Locate every blood parasite and identify its species.
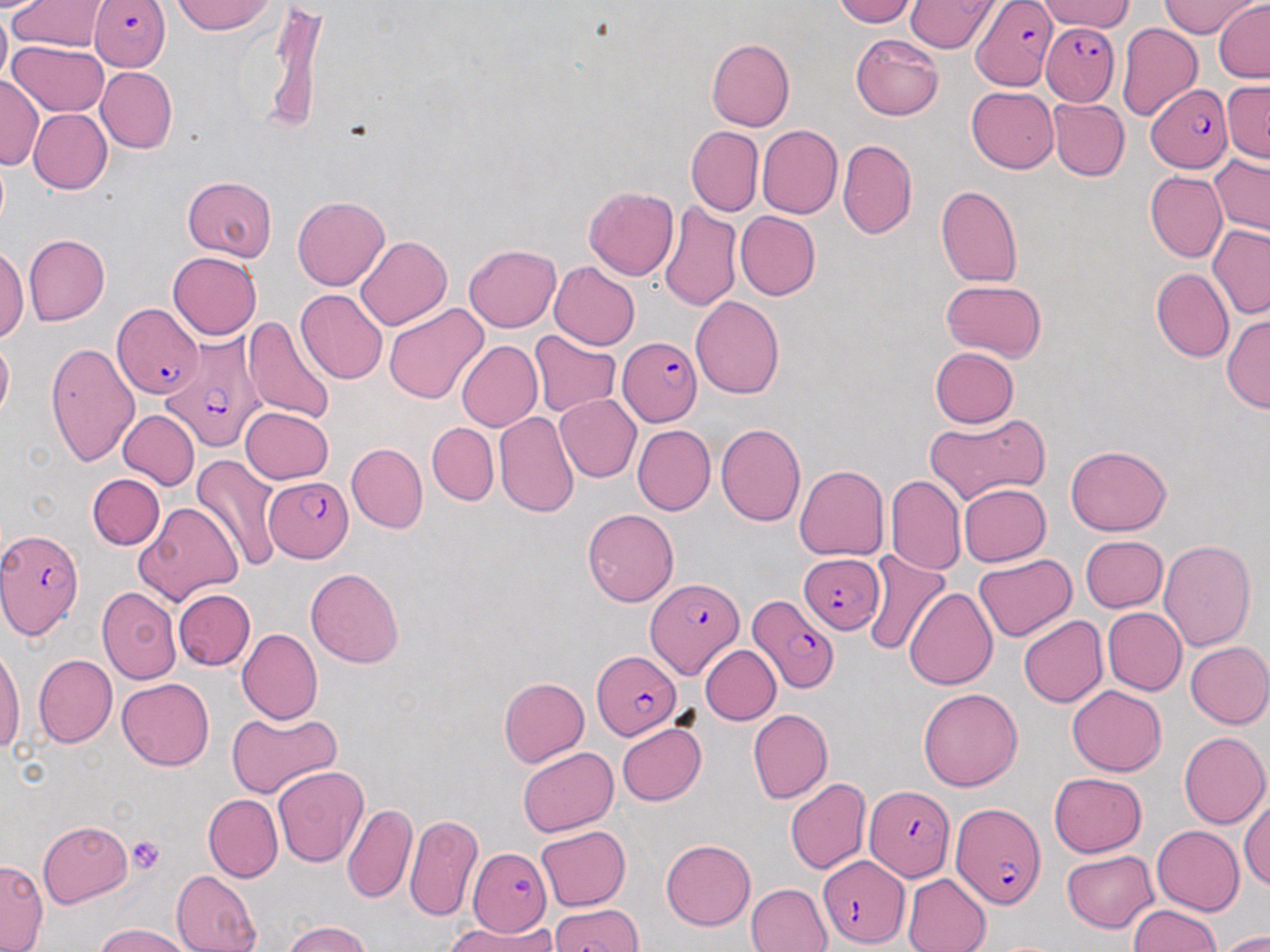

Approximate bounding boxes as (x1,y1)-(x2,y2) corner pairs in pixels.
Plasmodium falciparum-infected red blood cells: (970,0)-(1056,91), (91,1)-(171,72), (1040,20)-(1122,109), (1145,84)-(1234,173), (111,303)-(202,399), (160,336)-(264,453), (620,337)-(702,427), (267,478)-(353,559), (1,527)-(86,639), (798,553)-(884,633), (646,577)-(741,677), (748,592)-(839,693), (594,652)-(680,734), (865,786)-(952,882), (951,802)-(1046,907), (470,847)-(552,938), (820,855)-(909,948).
No Plasmodium ovale, Plasmodium malariae, Plasmodium vivax, Babesia divergens, or Trypanosoma brucei observed.

slide-level diagnosis = Plasmodium falciparum
image size = 1270×952 pixels
uninfected red blood cell locations = approximate bounding boxes as (x1,y1)-(x2,y2) corner pairs in pixels: (173,0)-(277,35), (833,0)-(918,26), (1161,0)-(1261,38), (1214,0)-(1270,82), (8,1)-(108,53), (905,1)-(998,52), (1035,2)-(1139,32), (0,4)-(11,91), (263,9)-(326,135), (1116,22)-(1203,121), (850,33)-(943,120), (706,38)-(794,131), (8,39)-(108,117), (96,66)-(177,154), (0,73)-(42,170), (1222,80)-(1270,163), (967,87)-(1058,173), (1048,97)-(1130,181), (28,109)-(112,194), (756,125)-(842,219), (685,126)-(764,216), (838,139)-(917,239), (1209,153)-(1270,236), (1145,171)-(1227,263), (183,177)-(277,260), (936,184)-(1022,287), (583,186)-(678,280), (293,196)-(389,290), (659,200)-(742,311), (735,211)-(821,300), (1207,225)-(1270,320), (23,235)-(109,326), (355,235)-(451,330), (464,243)-(561,332), (0,246)-(29,344), (167,251)-(262,340), (549,262)-(640,351), (1152,268)-(1234,362), (941,280)-(1047,360), (295,289)-(389,385), (689,295)-(785,398), (383,303)-(490,405), (1220,312)-(1270,414), (243,313)-(337,423), (530,331)-(620,418), (0,335)-(13,422), (44,340)-(139,469), (456,340)-(542,432), (928,346)-(1018,428), (555,395)-(641,482), (240,406)-(333,485), (118,409)-(200,490), (492,409)-(579,517), (923,414)-(1050,504), (427,423)-(499,505), (716,423)-(807,526), (632,425)-(716,515), (346,443)-(427,533), (1064,444)-(1172,536), (192,455)-(284,571), (794,464)-(889,561), (86,474)-(164,550), (885,475)-(965,576), (958,483)-(1050,566), (136,502)-(242,605), (582,508)-(679,606), (1080,535)-(1167,612), (1158,538)-(1256,652), (863,549)-(950,655), (973,555)-(1077,642), (305,567)-(405,668), (97,585)-(182,684), (903,587)-(998,689), (173,589)-(256,670), (1103,608)-(1187,695), (1018,615)-(1109,708), (237,628)-(324,724), (1184,641)-(1270,729), (1,643)-(24,753), (700,645)-(781,725), (33,654)-(117,748), (117,677)-(214,770), (498,677)-(589,768), (1066,686)-(1167,777), (918,688)-(1024,791), (747,709)-(832,803), (226,711)-(340,800), (617,723)-(707,805), (1179,731)-(1269,829), (517,747)-(618,835), (273,766)-(368,869), (1048,772)-(1148,858), (785,777)-(871,875), (203,794)-(283,882), (1240,797)-(1269,891), (342,802)-(417,905), (404,813)-(483,923), (38,821)-(132,907), (535,824)-(631,911), (1151,824)-(1244,915), (660,839)-(755,930), (1062,851)-(1157,932), (0,859)-(48,950), (171,869)-(261,952), (902,873)-(992,952), (746,882)-(832,952), (548,903)-(645,952), (1129,904)-(1221,952), (447,919)-(557,952), (281,921)-(375,952), (95,922)-(194,952), (1216,929)-(1270,951)
field of view = one of a larger specimen
modality = light microscopy
magnification = 1000x
preparation = thin blood smear
platelet locations = approximate bounding boxes as (x1,y1)-(x2,y2) corner pairs in pixels: (127,835)-(164,874)
stain = May-Grünwald-Giemsa